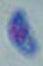
Toxoplasma gondii is shown. 1000x magnification. Micrograph.